Outline each uninfected red blood cell.
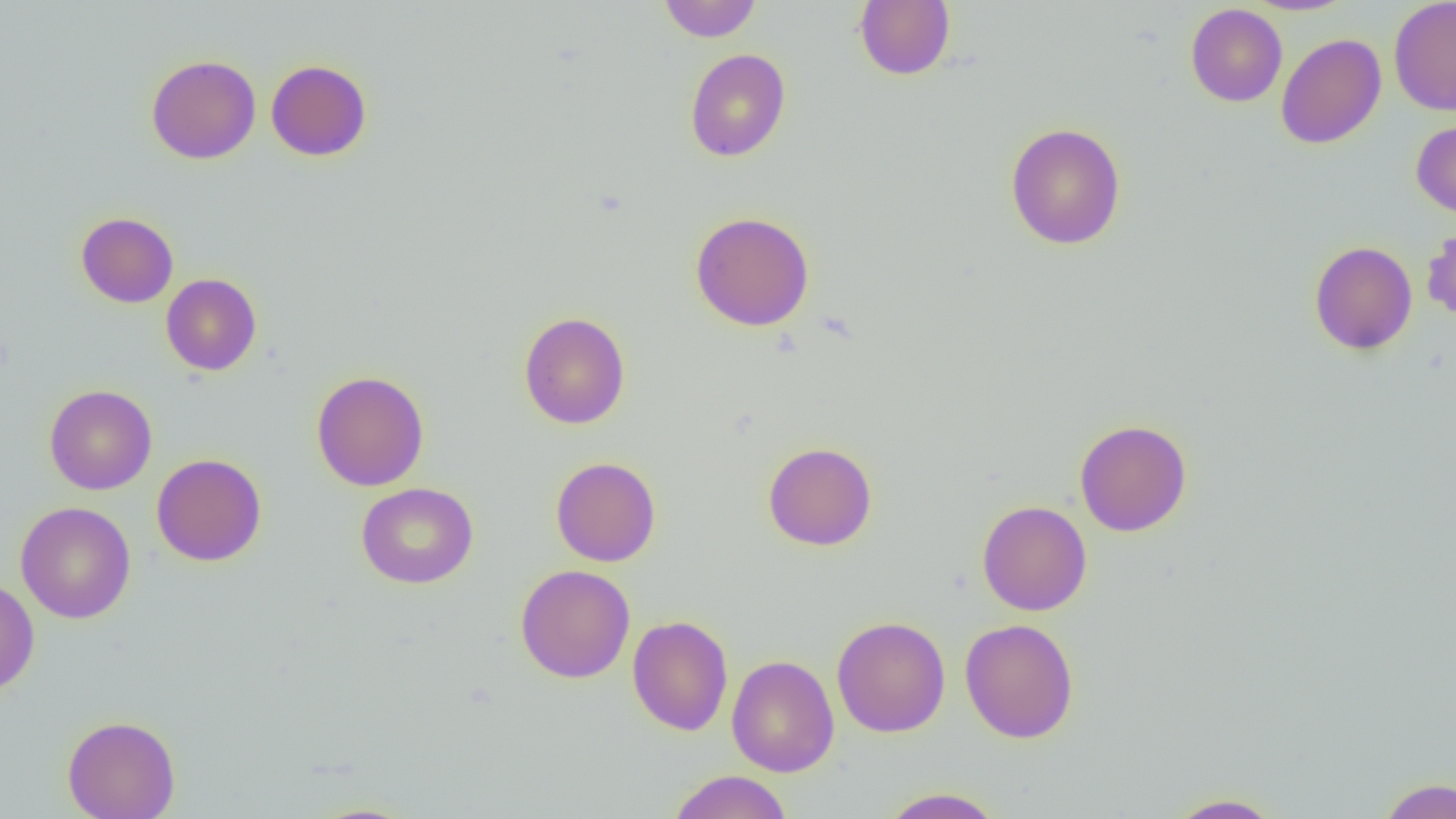
Approximate bounding boxes as named x1/y1/x2/y2 corners in pixels.
Uninfected red blood cells: (x1=658, y1=0, x2=762, y2=42), (x1=1388, y1=0, x2=1456, y2=116), (x1=854, y1=1, x2=955, y2=80), (x1=1186, y1=3, x2=1287, y2=107), (x1=1276, y1=33, x2=1386, y2=149), (x1=684, y1=48, x2=791, y2=162), (x1=146, y1=54, x2=261, y2=164), (x1=266, y1=59, x2=372, y2=161), (x1=1411, y1=120, x2=1456, y2=218), (x1=1005, y1=122, x2=1126, y2=250), (x1=690, y1=211, x2=815, y2=331), (x1=76, y1=212, x2=178, y2=308), (x1=1421, y1=223, x2=1456, y2=326), (x1=1309, y1=240, x2=1417, y2=355), (x1=161, y1=273, x2=262, y2=376), (x1=518, y1=311, x2=631, y2=429), (x1=311, y1=370, x2=429, y2=491), (x1=44, y1=384, x2=157, y2=495), (x1=1074, y1=419, x2=1192, y2=536), (x1=763, y1=441, x2=877, y2=551), (x1=152, y1=453, x2=267, y2=566), (x1=551, y1=456, x2=661, y2=566), (x1=356, y1=482, x2=478, y2=588), (x1=977, y1=500, x2=1092, y2=616), (x1=15, y1=501, x2=136, y2=624), (x1=516, y1=564, x2=635, y2=683), (x1=0, y1=579, x2=40, y2=695), (x1=627, y1=615, x2=733, y2=735), (x1=832, y1=615, x2=951, y2=738), (x1=960, y1=619, x2=1079, y2=743), (x1=726, y1=655, x2=839, y2=777), (x1=62, y1=715, x2=180, y2=819), (x1=668, y1=770, x2=793, y2=819), (x1=1376, y1=777, x2=1456, y2=818), (x1=878, y1=787, x2=1005, y2=818), (x1=1164, y1=792, x2=1286, y2=818).

{
  "slide_level_diagnosis": "negative for blood parasites",
  "modality": "light microscopy",
  "magnification": "1000x",
  "preparation": "thin blood smear",
  "image_size": "1456×819 pixels",
  "field_of_view": "one of a larger specimen"
}